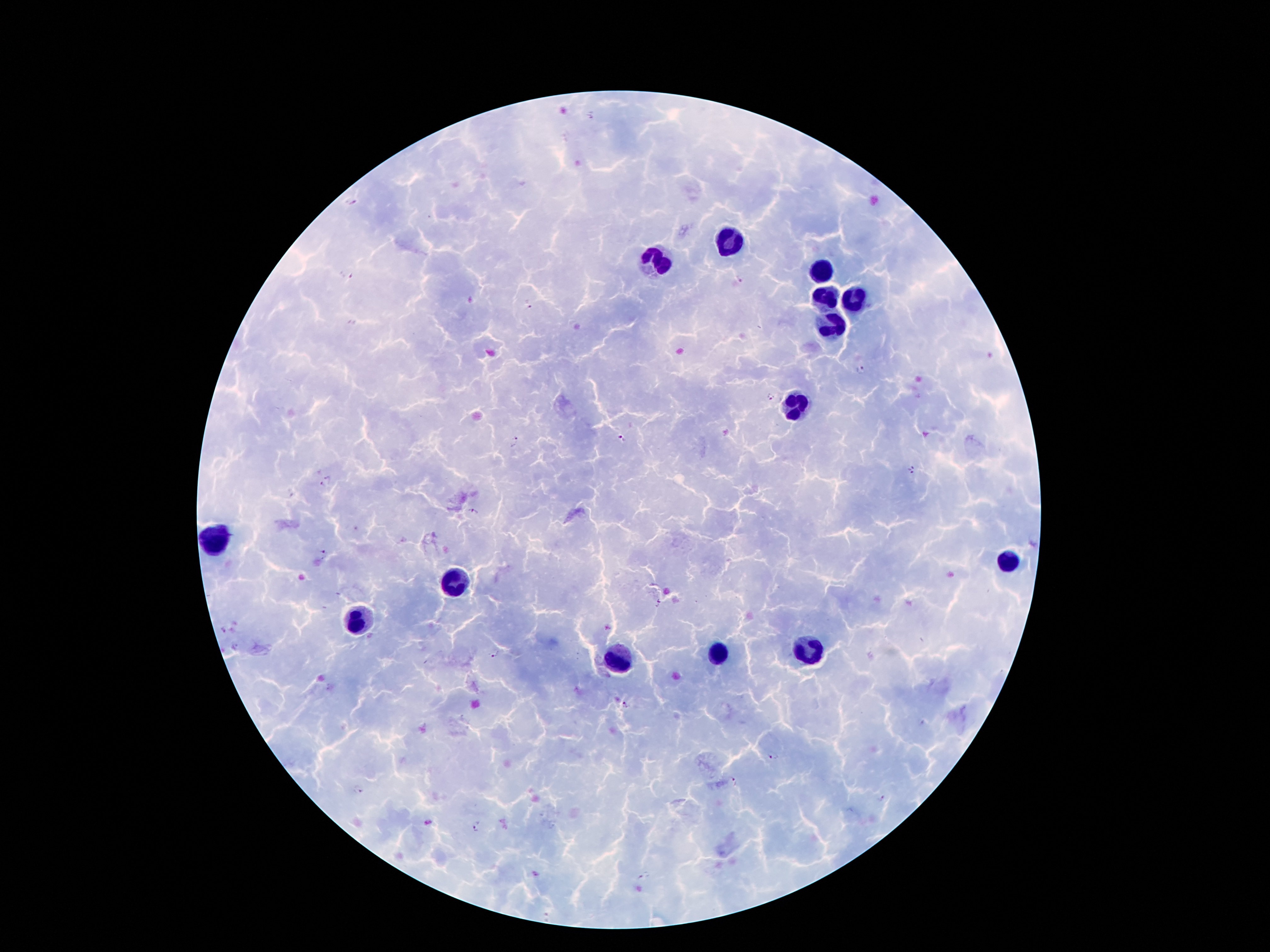

Approximate centers as [x, y] in pixels.
Summary:
  - Malaria parasite locations: [349, 201], [348, 276], [740, 277], [529, 309], [861, 368], [770, 396], [622, 439], [513, 441], [910, 470], [326, 483], [472, 512], [324, 554], [660, 604], [223, 630], [495, 654], [625, 706], [773, 757], [733, 782], [358, 789], [882, 800], [477, 827], [643, 875]
  - Leukocyte locations: [726, 243], [654, 261], [818, 273], [824, 297], [854, 301], [828, 325], [790, 406], [214, 538], [1006, 558], [456, 580], [360, 624], [808, 650], [718, 654], [618, 658]
  - Field of view: one from this slide
  - Patient malaria status: positive for Plasmodium falciparum
  - Image size: 1270×952 pixels
  - Capture: smartphone through the microscope eyepiece
  - Magnification: 100x
  - Stain: Giemsa
  - Preparation: thick peripheral-blood smear